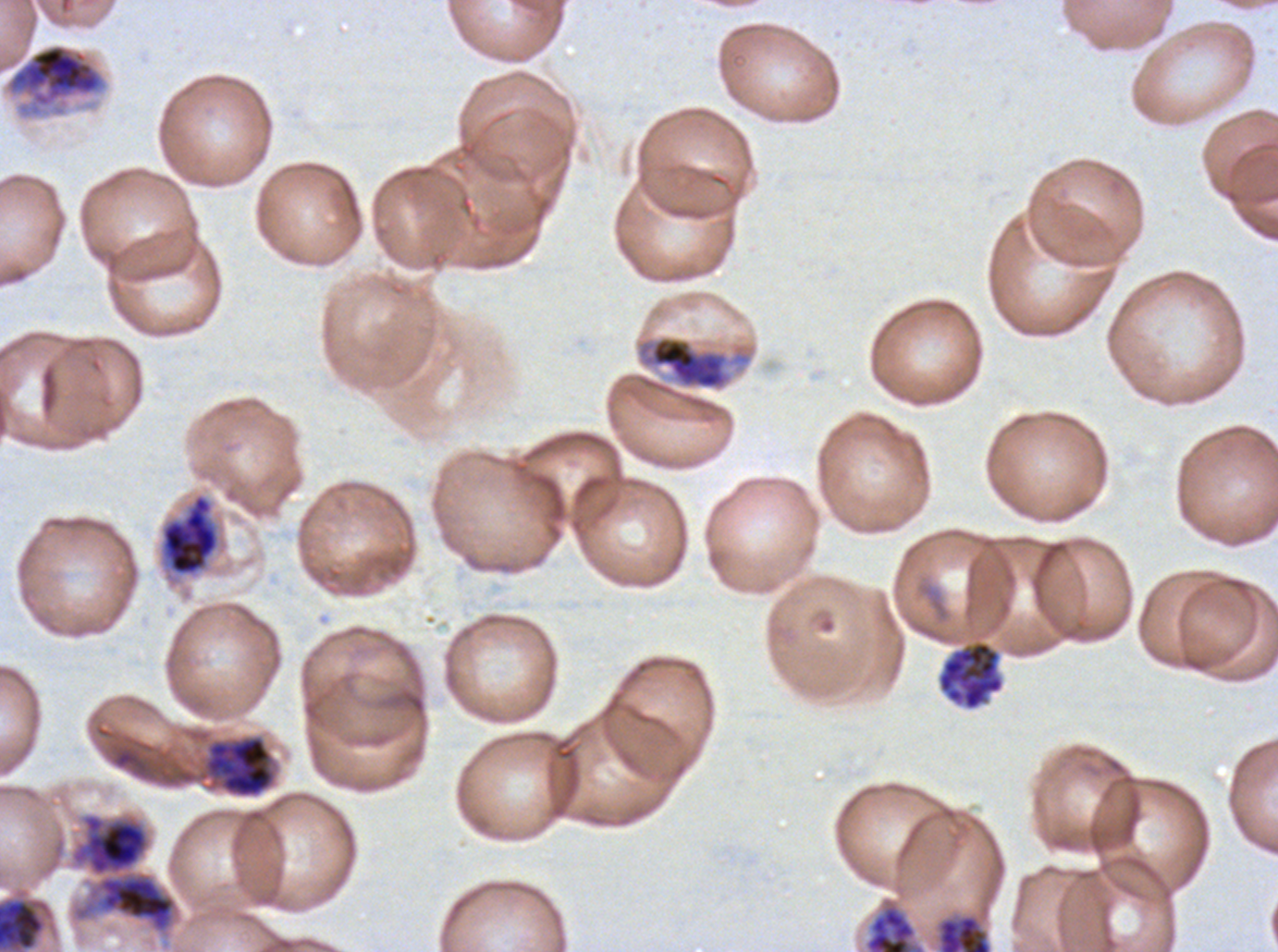

Approximate bounding rectangles given as corner coordinates in pixels from the top-left.
Summary:
  - Early schizont locations: (x1=635, y1=335, x2=752, y2=391), (x1=203, y1=735, x2=276, y2=799), (x1=70, y1=813, x2=177, y2=934), (x1=0, y1=900, x2=43, y2=950)
  - Late schizont locations: (x1=4, y1=43, x2=107, y2=119), (x1=159, y1=492, x2=221, y2=578), (x1=937, y1=641, x2=1004, y2=711), (x1=864, y1=901, x2=926, y2=951), (x1=938, y1=915, x2=991, y2=951)
  - Field of view: one sub-image of a larger composite
  - Life-cycle stages observed: early schizont, late schizont
  - Stain: Giemsa
  - Image size: 1278×952 pixels
  - Specimen: Plasmodium falciparum from a patient in The Gambia, cultured ex vivo for 24 to 48 hours
  - Preparation: thin blood smear